State which cell type is depicted.
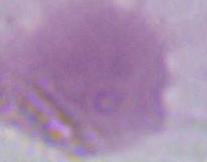

An erythrocyte.

modality = photomicrograph
magnification = 1000x